Assess the morphology of the erythrocytes.
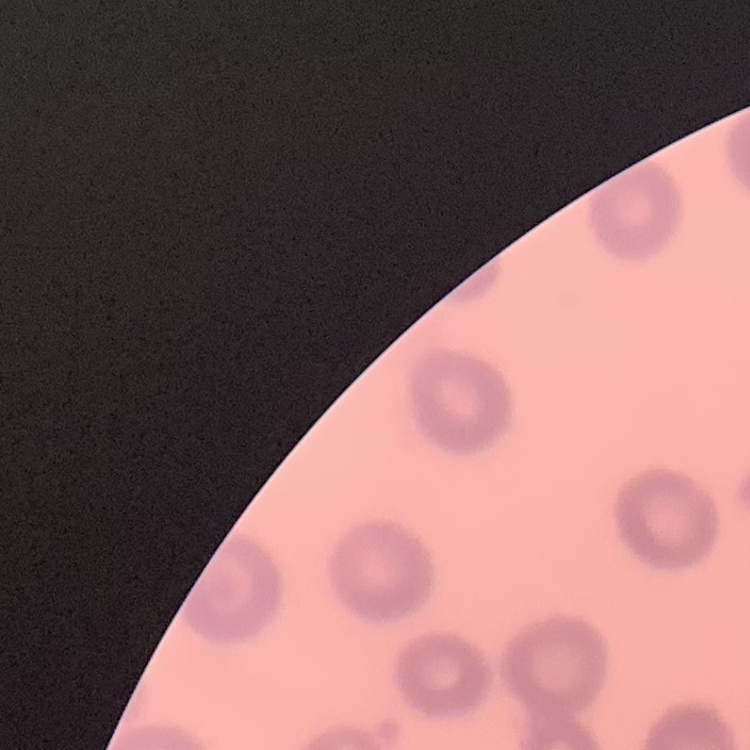
No rouleaux formation.

Summary:
  - Preparation: thin peripheral smear
  - Image type: square crop of a larger photomicrograph
  - Stain: Field's or Giemsa